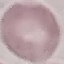
Summary:
  - Result: no malaria parasites detected
  - Image type: automatically extracted cell patch, resized to 64 × 64 pixels
  - Capture: smartphone through the microscope eyepiece
  - Preparation: thin blood film
  - Stain: Giemsa